State which parasite is depicted.
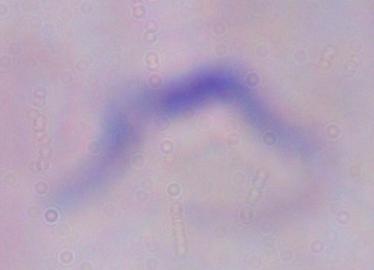
This is a trypanosome.

Micrograph. Captured at 1000x magnification.